Report the malaria status of this cell.
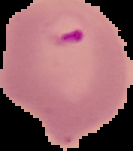

Parasitized.

{
  "preparation": "thin blood smear",
  "image_size": "133×151 pixels",
  "image_type": "segmented cell region on a black background"
}